Comment on the morphology of the erythrocytes.
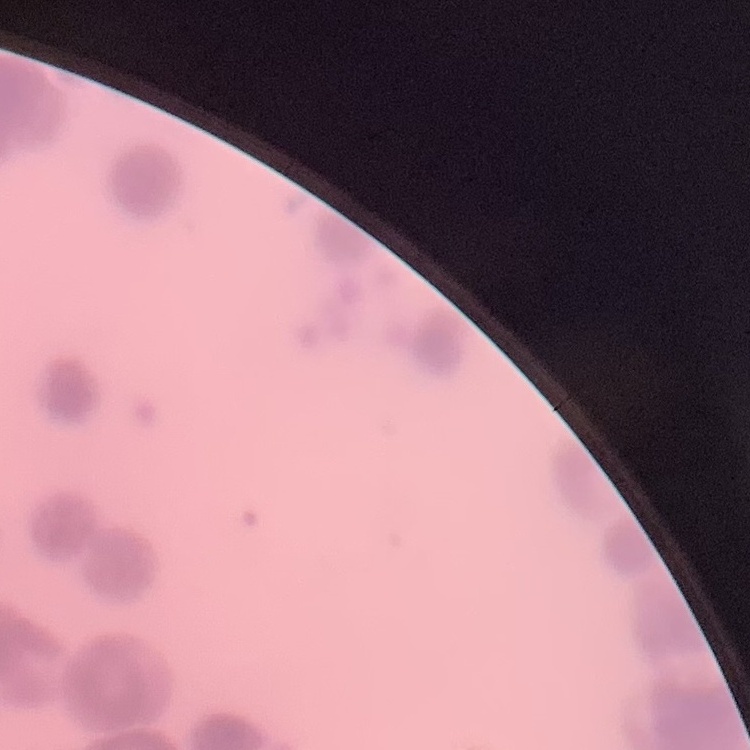

They show rouleaux formation.

Thin blood film. Field's or Giemsa stain. Square crop of a larger photomicrograph.